Report the malaria status.
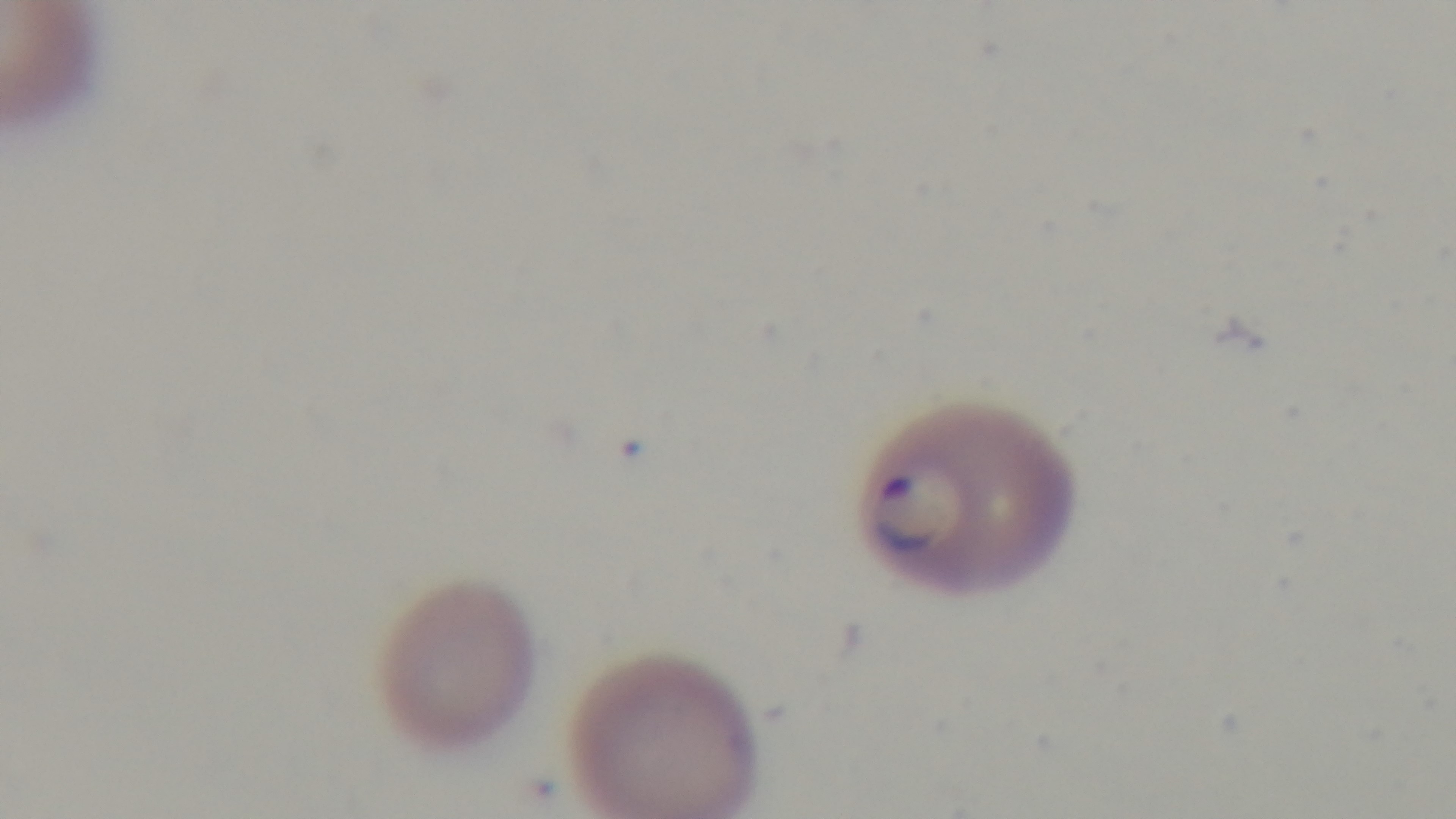

Positive.

capture = mounted 4K digital camera
modality = light microscopy
objective = 100x oil immersion
field of view = single
preparation = thin blood film
stain = Giemsa